Describe the morphology of the erythrocytes.
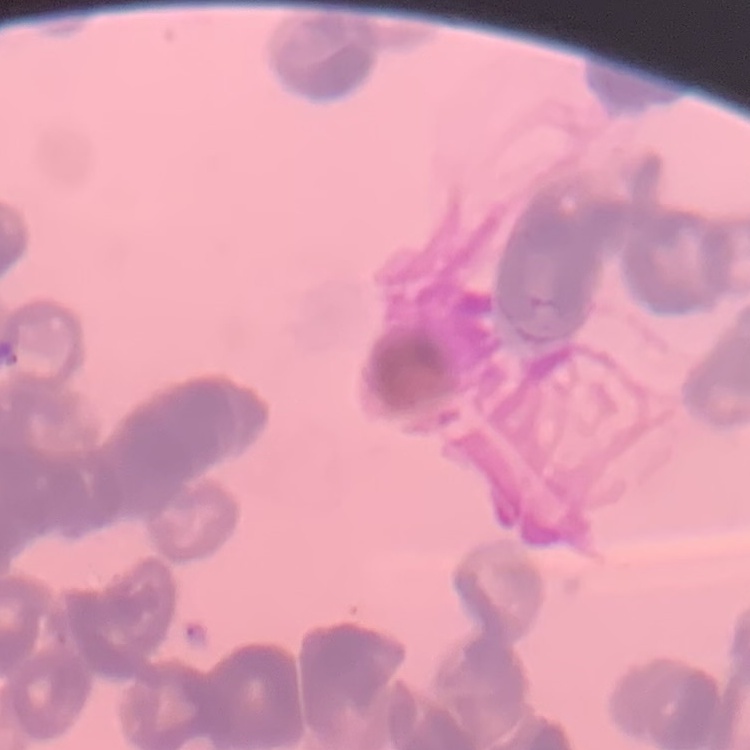

They show rouleaux formation.

Summary:
  - Stain: Field's or Giemsa
  - Preparation: thin blood film
  - Image type: square crop of a larger photomicrograph